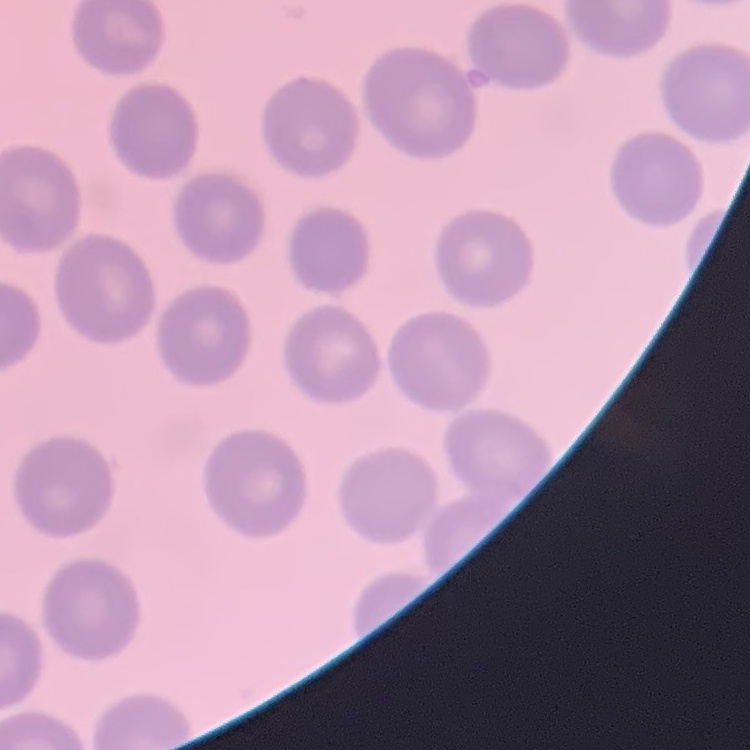
The red blood cells exhibit no rouleaux formation. Thin peripheral smear. Square crop of a larger photomicrograph. Stained with either Field's or Giemsa.